Point out each Plasmodium parasite.
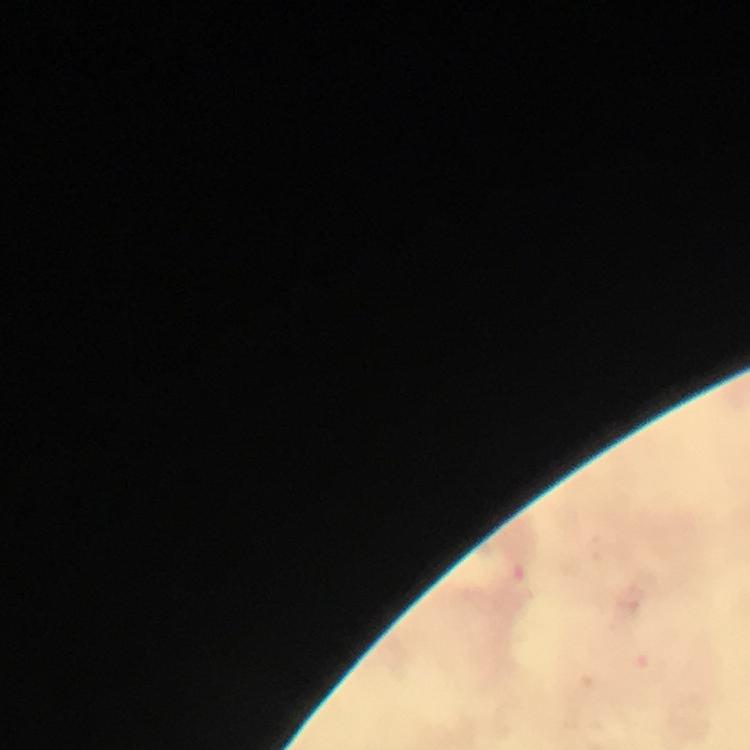

Approximate centers as [x, y] in pixels.
Plasmodium parasites: [651, 667].

magnification: 100x
stain: Giemsa
immersion_oil: used
capture: smartphone mounted on the microscope
preparation: thick blood film
cropped_from: a single field of view
context: from a diagnostic examination for malaria
image_size: 750×750 pixels